Classify this cell by malaria status.
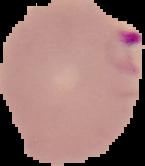
It is parasitized.

image size = 145×166 pixels
preparation = thin blood smear
image type = segmented cell region with the area outside set to black